Assess this cell for malaria.
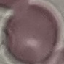
It is uninfected.

Summary:
  - Capture: smartphone through the microscope eyepiece
  - Image type: cell patch, automatically extracted from a larger field of view and resized to 64 × 64 pixels
  - Stain: Giemsa
  - Preparation: thin blood smear